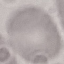
malaria status = uninfected
preparation = thin smear
stain = Giemsa
capture = smartphone through the microscope eyepiece
image type = automatically extracted cell patch, resized to 64 × 64 pixels